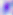

Photomicrograph. Toxoplasma gondii is seen. 400x magnification.